Classify this cell by malaria status.
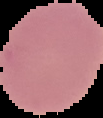

It is uninfected.

Cell region segmented out of the field of view; the surrounding area is masked to black. From a thin blood film. Image is 103×118 pixels.